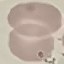

{
  "malaria_status": "uninfected",
  "capture": "smartphone through the microscope eyepiece",
  "image_type": "cell patch, automatically extracted from a larger field of view and resized to 64 × 64 pixels",
  "stain": "Giemsa",
  "preparation": "thin blood smear"
}